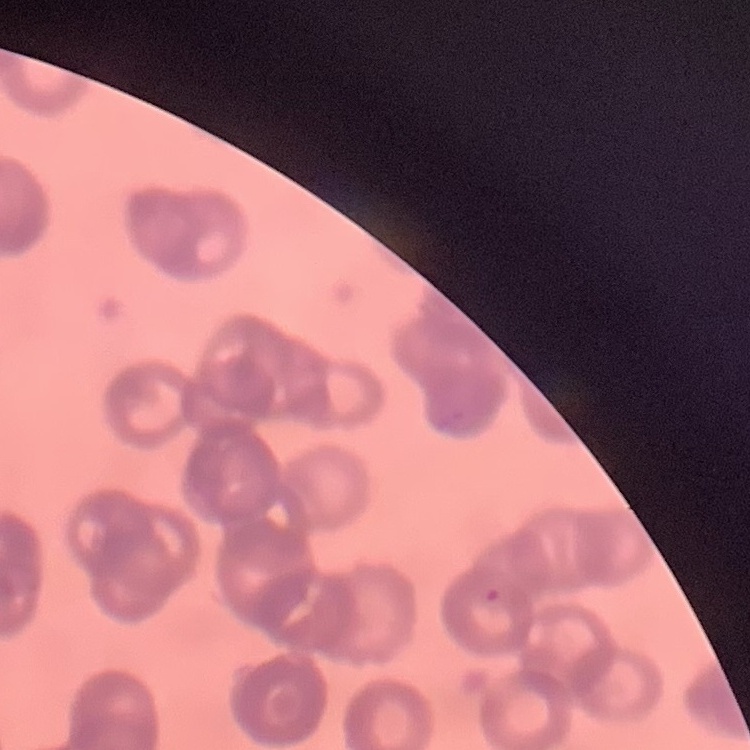
red blood cell morphology = rouleaux formation
preparation = thin blood film
image type = one tile cut from a larger photomicrograph
stain = Field's or Giemsa